State which cell type is depicted.
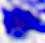
This is a leukocyte.

Summary:
  - Magnification: 400x
  - Modality: micrograph